Classify this cell by malaria status.
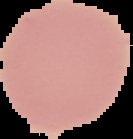

Uninfected.

{
  "preparation": "thin blood smear",
  "image_size": "133×139 pixels",
  "image_type": "cell region segmented out of the field of view; surrounding area masked to black"
}